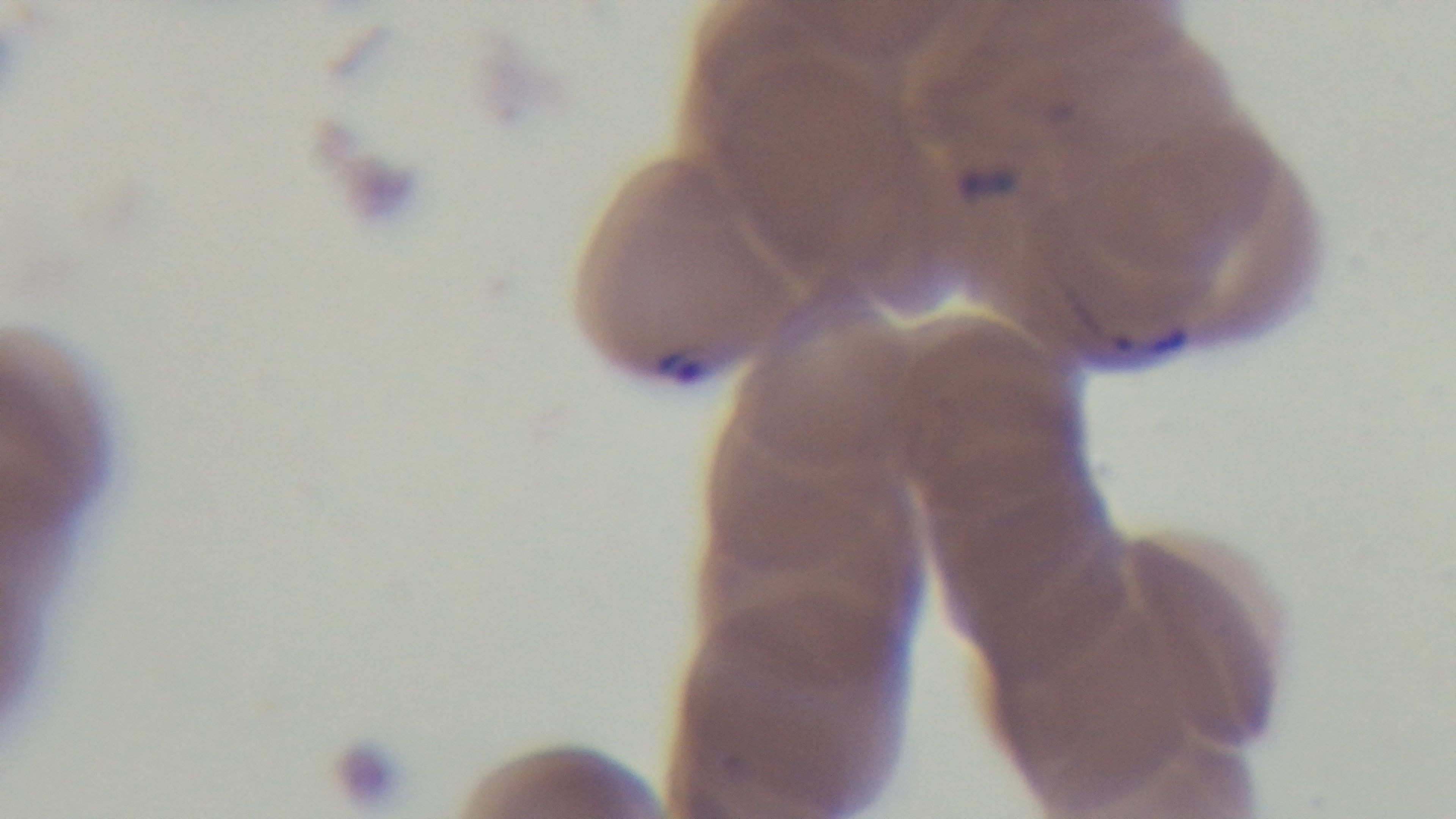
One field from the slide. 100x oil-immersion objective. Malaria status: positive. Giemsa stain. Preparation: thin. Mounted 4K digital camera. Photomicrograph.